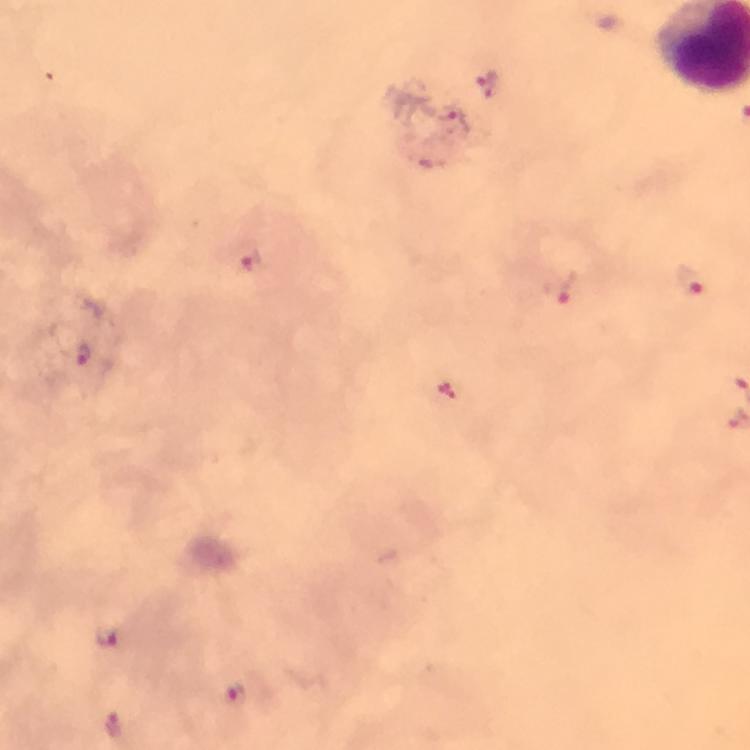
preparation = thick blood smear
image size = 750×750 pixels
cropped from = a single field of view
stain = Giemsa
Plasmodium parasite locations = approximate centers as {x, y} in pixels: {252, 261}, {689, 279}, {560, 286}, {84, 354}, {107, 636}, {233, 693}, {114, 724}
magnification = 100x
context = from a diagnostic examination for malaria
immersion oil = applied
capture = smartphone mounted on the microscope